Report the malaria status of this cell.
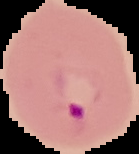
Parasitized.

Image is 139×154 pixels. From a thin blood smear. The area outside the segmented cell region is set to black.